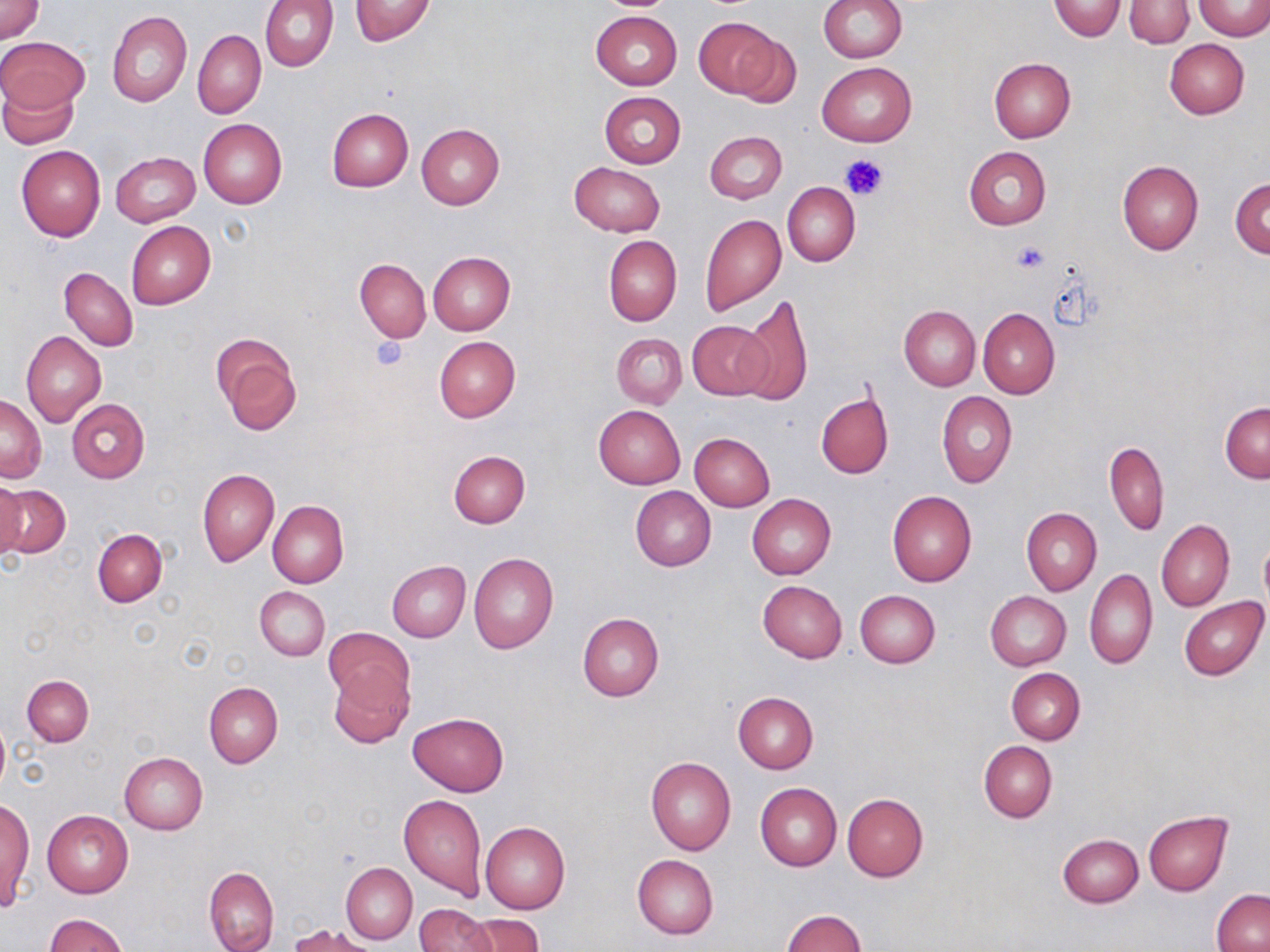
Approximate bounding boxes as [x1, y1, x2, y2] in pixels. Uninfected red blood cell locations: [0, 0, 44, 43], [258, 0, 337, 72], [349, 0, 435, 45], [818, 0, 906, 63], [1050, 0, 1124, 40], [593, 1, 684, 12], [1124, 1, 1193, 48], [1194, 1, 1269, 40], [107, 11, 192, 107], [591, 11, 681, 90], [693, 16, 781, 98], [193, 29, 265, 118], [731, 32, 802, 110], [1, 37, 87, 114], [1164, 39, 1249, 118], [988, 57, 1076, 142], [816, 61, 917, 147], [0, 77, 81, 148], [599, 91, 685, 169], [327, 109, 413, 191], [198, 119, 287, 208], [416, 123, 505, 210], [704, 130, 787, 203], [16, 145, 106, 242], [963, 146, 1051, 230], [111, 152, 199, 227], [1117, 160, 1204, 254], [569, 162, 666, 237], [1230, 178, 1270, 257], [782, 182, 860, 268], [700, 214, 787, 316], [126, 221, 215, 310], [604, 235, 681, 326], [428, 251, 516, 336], [354, 258, 431, 342], [60, 267, 138, 351], [737, 294, 813, 405], [900, 306, 981, 390], [978, 307, 1059, 399], [688, 320, 771, 399], [21, 331, 106, 425], [611, 333, 687, 409], [212, 335, 302, 435], [434, 336, 520, 421], [816, 390, 893, 480], [937, 391, 1017, 488], [1, 394, 46, 482], [67, 398, 149, 483], [1220, 402, 1270, 482], [593, 405, 684, 490], [689, 433, 775, 511], [1104, 440, 1168, 535], [448, 450, 530, 527], [198, 468, 279, 567], [0, 481, 26, 563], [1, 483, 70, 559], [630, 486, 716, 571], [887, 491, 977, 586], [747, 494, 835, 579], [267, 499, 348, 589], [1021, 507, 1101, 596], [1156, 520, 1234, 611], [92, 528, 167, 606], [1259, 535, 1270, 616], [468, 553, 558, 655], [387, 561, 471, 641], [1084, 568, 1157, 668], [758, 580, 847, 663], [255, 586, 329, 661], [854, 590, 940, 668], [984, 591, 1071, 670], [1178, 597, 1269, 680], [577, 613, 664, 701], [323, 627, 413, 710], [328, 666, 413, 747], [1007, 668, 1085, 745], [22, 675, 93, 746], [203, 682, 283, 768], [733, 691, 819, 773], [408, 712, 508, 797], [0, 713, 10, 797], [979, 741, 1057, 821], [119, 752, 207, 835], [646, 757, 736, 856], [755, 783, 841, 872], [398, 793, 486, 899], [842, 794, 928, 882], [2, 798, 33, 906], [42, 809, 134, 897], [1142, 811, 1232, 896], [482, 822, 570, 914], [1058, 834, 1144, 908], [632, 854, 719, 938], [341, 862, 417, 943], [204, 867, 279, 952], [1211, 889, 1269, 952], [415, 902, 498, 952], [782, 909, 866, 952], [47, 914, 129, 952], [464, 914, 544, 952], [293, 925, 377, 952]. Platelet locations: [841, 154, 887, 202], [1011, 241, 1051, 272], [369, 335, 409, 372]. Slide-level diagnosis: no evidence of blood parasites. Thin blood smear. Image is 1270×952 pixels. May-Grünwald-Giemsa stain. Single field of view. Light microscopy. Captured at 1000x magnification.